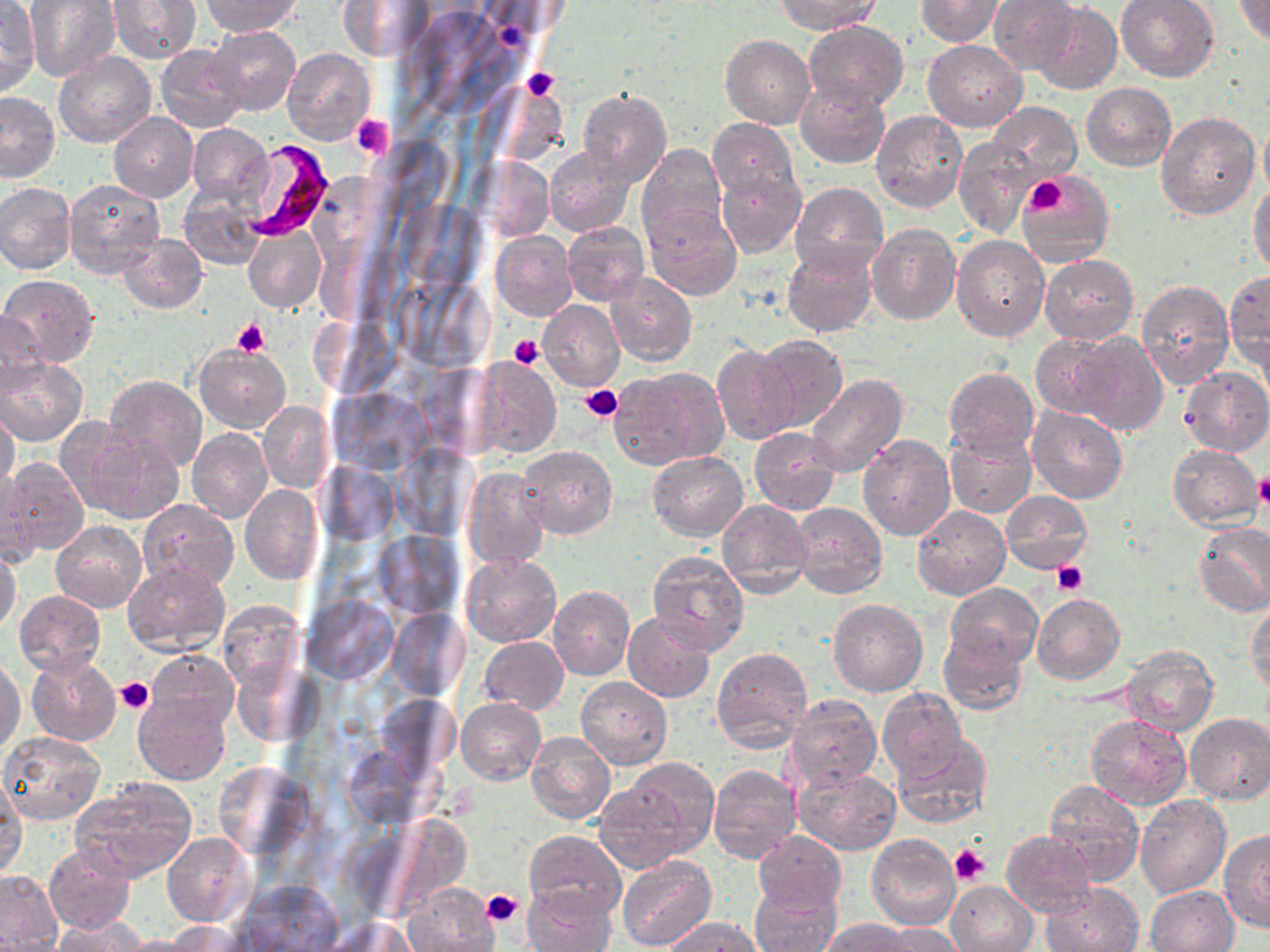
slide-level diagnosis = Plasmodium falciparum
uninfected red blood cell locations = approximate bounding boxes as (x1, y1, x2, y2) in pixels: (25, 0, 119, 81), (107, 0, 201, 67), (204, 0, 300, 35), (776, 0, 880, 34), (917, 0, 1001, 45), (988, 0, 1080, 74), (1116, 0, 1219, 82), (1234, 0, 1270, 47), (336, 1, 434, 61), (0, 2, 39, 98), (1031, 4, 1122, 95), (803, 20, 909, 111), (210, 26, 300, 116), (721, 35, 814, 129), (922, 39, 1028, 132), (156, 44, 246, 133), (282, 48, 374, 146), (53, 52, 156, 149), (796, 82, 890, 169), (1081, 83, 1174, 170), (577, 88, 670, 186), (0, 92, 60, 182), (989, 102, 1080, 182), (870, 110, 967, 214), (1156, 111, 1260, 219), (109, 112, 198, 202), (707, 118, 798, 205), (1258, 118, 1270, 201), (186, 123, 272, 206), (954, 136, 1037, 239), (637, 144, 727, 247), (544, 146, 634, 236), (715, 165, 805, 258), (1020, 171, 1113, 265), (65, 179, 166, 279), (0, 182, 77, 274), (790, 182, 886, 276), (1250, 184, 1270, 280), (179, 185, 267, 271), (644, 204, 742, 301), (563, 222, 649, 305), (866, 223, 961, 326), (244, 229, 325, 312), (491, 231, 578, 320), (119, 234, 208, 313), (952, 235, 1048, 342), (782, 241, 878, 339), (1039, 253, 1137, 343), (605, 273, 696, 365), (1226, 273, 1270, 372), (2, 275, 100, 367), (1135, 281, 1234, 390), (538, 300, 625, 390), (1, 309, 46, 397), (1029, 333, 1120, 419), (1073, 333, 1167, 436), (755, 336, 848, 433), (712, 342, 801, 444), (195, 344, 290, 433), (646, 353, 791, 453), (472, 356, 560, 457), (0, 357, 86, 446), (614, 367, 728, 468), (944, 368, 1038, 457), (1180, 368, 1270, 456), (805, 374, 908, 478), (103, 375, 207, 475), (258, 402, 334, 494), (0, 407, 21, 493), (1026, 407, 1127, 504), (65, 424, 182, 527), (750, 426, 842, 517), (188, 428, 272, 523), (945, 429, 1035, 518), (859, 434, 956, 540), (1168, 444, 1261, 530), (517, 446, 617, 539), (647, 451, 747, 540), (2, 457, 89, 559), (0, 467, 41, 565), (461, 467, 548, 570), (239, 485, 323, 584), (1000, 490, 1091, 573), (136, 499, 239, 592), (718, 500, 814, 599), (789, 501, 886, 599), (912, 505, 1010, 599), (51, 521, 147, 613), (1194, 523, 1270, 616), (0, 547, 22, 634), (647, 549, 750, 654), (462, 553, 561, 647), (123, 562, 232, 657), (944, 582, 1042, 669), (548, 585, 634, 681), (14, 591, 106, 676), (1033, 592, 1126, 684), (1246, 596, 1270, 692), (828, 598, 928, 696), (217, 600, 307, 694), (624, 612, 715, 701), (938, 631, 1026, 716), (479, 637, 568, 714), (1121, 646, 1218, 736), (147, 648, 239, 731), (711, 648, 813, 753), (25, 655, 121, 747), (0, 660, 25, 755), (577, 676, 672, 769), (878, 687, 969, 783), (134, 693, 231, 784), (785, 693, 882, 790), (457, 699, 545, 783), (1183, 713, 1270, 804), (1085, 714, 1191, 809), (526, 732, 616, 825), (0, 733, 104, 822), (891, 733, 992, 829), (619, 756, 721, 857), (707, 764, 801, 863), (792, 764, 901, 855), (0, 777, 27, 879), (72, 777, 197, 882), (593, 778, 694, 872), (1041, 780, 1143, 884), (1136, 796, 1231, 897), (1219, 830, 1270, 933), (524, 831, 626, 919), (752, 831, 845, 916), (1000, 831, 1095, 916), (164, 832, 255, 926), (867, 834, 961, 930), (43, 844, 136, 935), (617, 857, 715, 951), (0, 870, 64, 950), (232, 880, 344, 952), (946, 881, 1037, 951), (1040, 881, 1144, 952), (402, 882, 496, 952), (750, 882, 841, 952), (521, 883, 617, 952), (1145, 885, 1239, 951), (52, 917, 146, 952), (659, 917, 763, 951), (820, 918, 918, 951), (318, 919, 422, 952), (164, 922, 252, 951), (873, 924, 960, 952), (117, 935, 211, 952)
preparation = thin blood film
Plasmodium falciparum-infected red blood cell locations = approximate bounding boxes as (x1, y1, x2, y2) in pixels: (236, 139, 333, 240)
modality = light microscopy
stain = May-Grünwald-Giemsa
image size = 1270×952 pixels
platelet locations = approximate bounding boxes as (x1, y1, x2, y2) in pixels: (521, 68, 560, 101), (350, 114, 394, 159), (1024, 176, 1068, 215), (231, 318, 270, 355), (509, 334, 546, 371), (581, 385, 622, 421), (1254, 474, 1270, 509), (1052, 561, 1089, 596), (115, 676, 155, 714), (950, 845, 989, 888), (482, 889, 523, 927)
magnification = 1000x
field of view = single